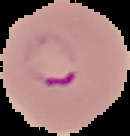

image_type: cell region segmented out of the field of view; surrounding area masked to black
preparation: thin blood smear
result: Plasmodium parasites detected
image_size: 130×136 pixels